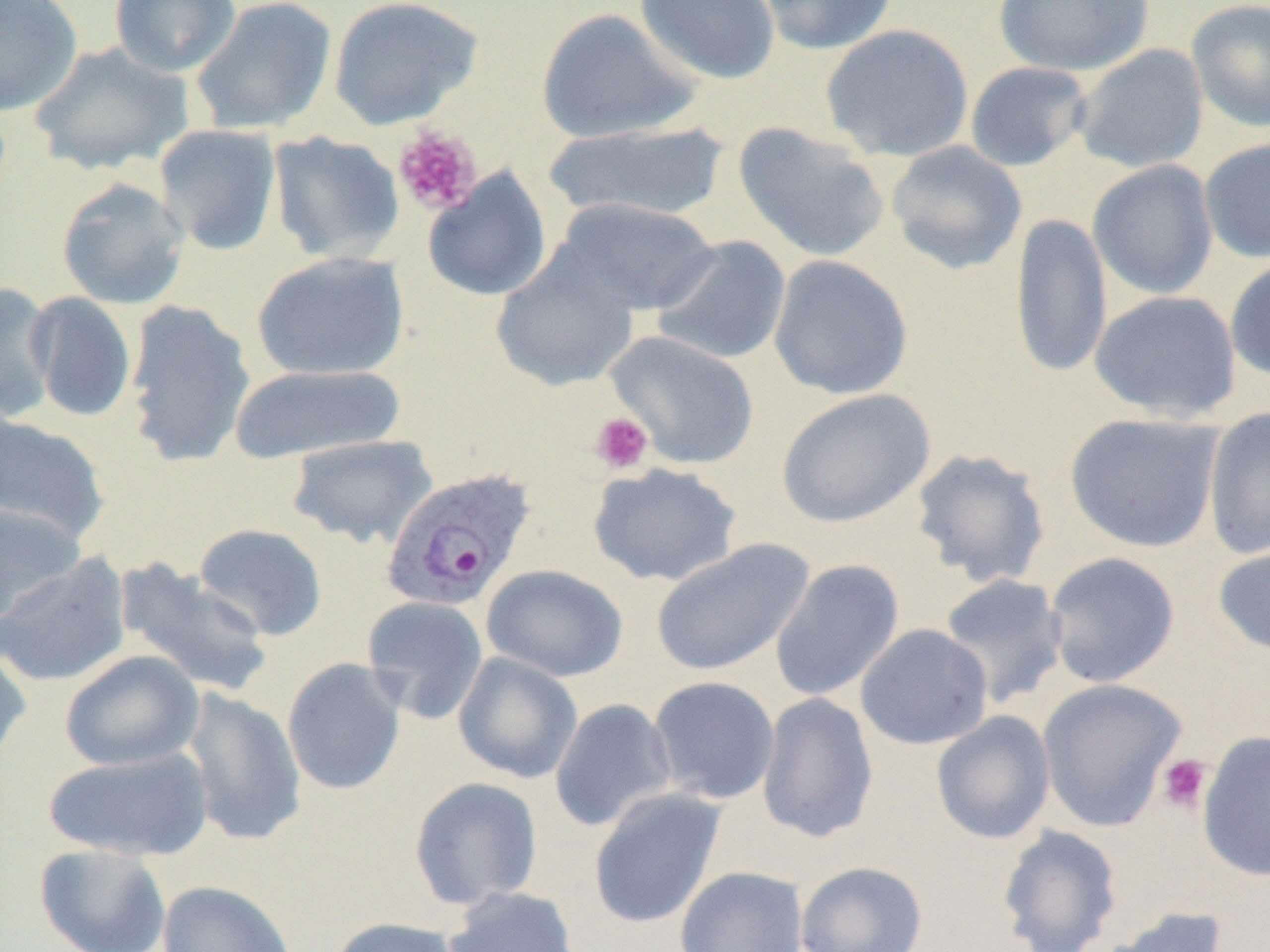
slide-level diagnosis = Plasmodium ovale
uninfected red blood cell locations (subset) = approximate bounding boxes as [x1, y1, x2, y2] in pixels: [0, 0, 83, 117], [109, 0, 242, 78], [190, 0, 336, 136], [327, 0, 483, 130], [634, 0, 781, 85], [754, 0, 899, 56], [992, 0, 1155, 76], [1186, 0, 1270, 133], [535, 7, 700, 144], [820, 23, 975, 162], [29, 41, 194, 176], [1071, 43, 1209, 174], [965, 61, 1093, 172], [541, 121, 730, 224], [733, 122, 890, 263], [154, 124, 282, 256], [268, 131, 406, 265], [1200, 137, 1270, 264], [885, 141, 1027, 275], [1088, 160, 1218, 299], [422, 167, 552, 301], [56, 177, 189, 310], [553, 197, 720, 316], [1010, 211, 1112, 380], [651, 236, 791, 366], [490, 250, 640, 392], [251, 251, 410, 381], [768, 255, 914, 400], [1224, 256, 1270, 383], [0, 282, 59, 423], [1089, 290, 1242, 422], [26, 292, 137, 422], [124, 299, 256, 468], [229, 363, 407, 464], [775, 388, 936, 528], [1202, 406, 1270, 559], [1064, 413, 1224, 553], [0, 414, 111, 543], [286, 434, 437, 549], [911, 448, 1051, 589], [587, 463, 743, 587], [0, 502, 86, 627], [193, 523, 328, 641], [1212, 538, 1270, 658], [650, 539, 814, 677], [1043, 551, 1181, 689], [0, 553, 133, 687], [113, 558, 274, 698], [769, 559, 904, 702], [481, 564, 628, 682], [937, 573, 1069, 708], [362, 596, 489, 724], [855, 624, 994, 750], [0, 641, 32, 765], [59, 650, 204, 772], [453, 652, 583, 783], [282, 657, 407, 795], [647, 675, 780, 805], [1036, 678, 1187, 832], [179, 687, 307, 847], [756, 692, 879, 844], [549, 698, 678, 833], [931, 711, 1056, 845], [1197, 730, 1270, 881], [43, 745, 214, 862], [409, 777, 544, 911], [588, 787, 727, 929], [997, 825, 1123, 952], [34, 843, 171, 952], [794, 860, 929, 952], [675, 865, 809, 952], [157, 880, 297, 952], [442, 886, 580, 952], [1100, 906, 1229, 952], [328, 916, 465, 952]
image size = 1270×952 pixels
field of view = single
preparation = thin blood smear
Plasmodium ovale-infected red blood cell locations = approximate bounding boxes as [x1, y1, x2, y2] in pixels: [380, 469, 536, 612]
modality = optical microscopy
magnification = 1000x
platelet locations (subset) = approximate bounding boxes as [x1, y1, x2, y2] in pixels: [392, 127, 482, 216], [590, 411, 653, 475], [1156, 754, 1212, 814]